Outline each Plasmodium falciparum-infected red blood cell.
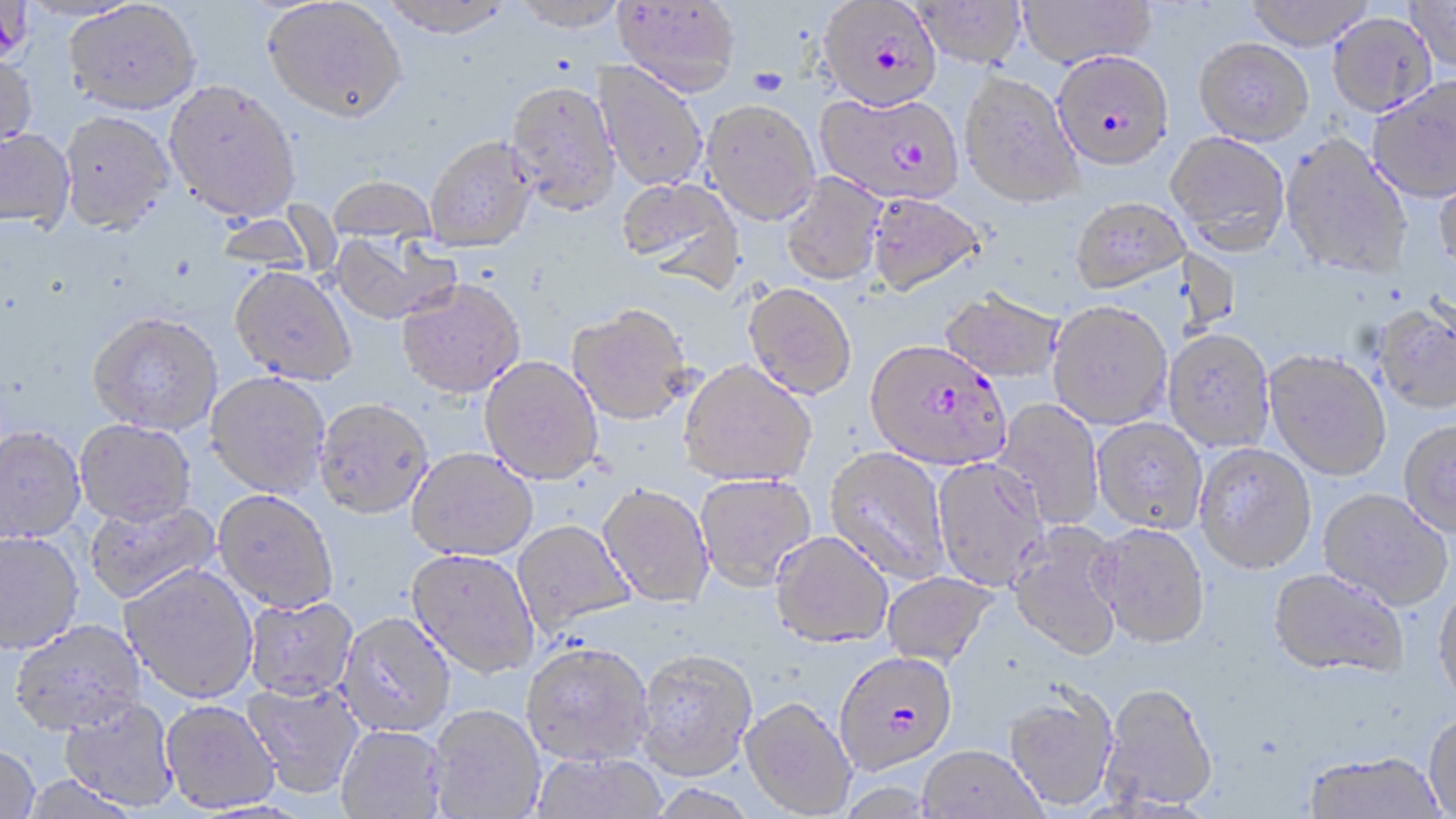

Approximate bounding boxes as named x1/y1/x2/y2 corners in pixels.
Plasmodium falciparum-infected red blood cells: (x1=818, y1=0, x2=942, y2=112), (x1=1055, y1=50, x2=1170, y2=169), (x1=815, y1=91, x2=965, y2=204), (x1=866, y1=340, x2=1011, y2=470), (x1=834, y1=651, x2=959, y2=775).

slide-level diagnosis = Plasmodium falciparum
stain = May-Grünwald-Giemsa
magnification = 1000x
preparation = thin blood smear
uninfected red blood cell locations = approximate bounding boxes as named x1/y1/x2/y2 corners in pixels: (x1=263, y1=0, x2=408, y2=124), (x1=377, y1=0, x2=515, y2=40), (x1=509, y1=0, x2=630, y2=34), (x1=613, y1=0, x2=740, y2=98), (x1=1017, y1=0, x2=1156, y2=68), (x1=1243, y1=0, x2=1376, y2=49), (x1=64, y1=1, x2=201, y2=114), (x1=913, y1=1, x2=1027, y2=69), (x1=1407, y1=1, x2=1455, y2=73), (x1=1328, y1=12, x2=1436, y2=117), (x1=1194, y1=36, x2=1313, y2=144), (x1=0, y1=52, x2=37, y2=155), (x1=593, y1=62, x2=708, y2=192), (x1=959, y1=70, x2=1082, y2=207), (x1=1367, y1=75, x2=1456, y2=203), (x1=163, y1=80, x2=301, y2=223), (x1=505, y1=82, x2=620, y2=217), (x1=702, y1=100, x2=821, y2=226), (x1=58, y1=111, x2=176, y2=234), (x1=0, y1=129, x2=76, y2=233), (x1=1166, y1=131, x2=1291, y2=255), (x1=1281, y1=134, x2=1413, y2=278), (x1=425, y1=137, x2=537, y2=253), (x1=1434, y1=164, x2=1456, y2=272), (x1=781, y1=172, x2=886, y2=286), (x1=328, y1=176, x2=437, y2=244), (x1=618, y1=178, x2=744, y2=290), (x1=867, y1=193, x2=987, y2=296), (x1=1070, y1=196, x2=1191, y2=293), (x1=329, y1=231, x2=460, y2=326), (x1=230, y1=267, x2=356, y2=385), (x1=397, y1=279, x2=526, y2=399), (x1=742, y1=283, x2=857, y2=400), (x1=940, y1=289, x2=1064, y2=382), (x1=1047, y1=300, x2=1173, y2=429), (x1=1373, y1=303, x2=1456, y2=413), (x1=568, y1=305, x2=693, y2=425), (x1=88, y1=314, x2=223, y2=436), (x1=1164, y1=328, x2=1276, y2=452), (x1=1265, y1=350, x2=1391, y2=480), (x1=479, y1=356, x2=604, y2=486), (x1=679, y1=361, x2=817, y2=487), (x1=205, y1=373, x2=330, y2=499), (x1=992, y1=398, x2=1105, y2=530), (x1=313, y1=399, x2=433, y2=522), (x1=1092, y1=417, x2=1208, y2=533), (x1=1399, y1=419, x2=1456, y2=537), (x1=75, y1=421, x2=197, y2=528), (x1=0, y1=428, x2=86, y2=544), (x1=1194, y1=443, x2=1316, y2=574), (x1=825, y1=447, x2=950, y2=583), (x1=407, y1=449, x2=538, y2=563), (x1=932, y1=457, x2=1049, y2=590), (x1=695, y1=473, x2=817, y2=591), (x1=597, y1=484, x2=714, y2=609), (x1=1319, y1=488, x2=1453, y2=610), (x1=213, y1=492, x2=338, y2=614), (x1=86, y1=499, x2=221, y2=605), (x1=512, y1=520, x2=635, y2=636), (x1=1007, y1=521, x2=1126, y2=660), (x1=1091, y1=523, x2=1211, y2=648), (x1=770, y1=531, x2=894, y2=648), (x1=0, y1=533, x2=83, y2=654), (x1=405, y1=550, x2=540, y2=680), (x1=120, y1=565, x2=259, y2=705), (x1=1268, y1=569, x2=1408, y2=679), (x1=882, y1=571, x2=998, y2=667), (x1=1433, y1=583, x2=1456, y2=710), (x1=244, y1=596, x2=359, y2=702), (x1=336, y1=614, x2=457, y2=739), (x1=8, y1=620, x2=146, y2=737), (x1=521, y1=642, x2=653, y2=766), (x1=634, y1=648, x2=758, y2=781), (x1=242, y1=679, x2=366, y2=800), (x1=1099, y1=682, x2=1219, y2=811), (x1=1003, y1=686, x2=1118, y2=812), (x1=741, y1=696, x2=857, y2=817), (x1=58, y1=698, x2=180, y2=812), (x1=160, y1=701, x2=281, y2=814), (x1=428, y1=706, x2=546, y2=819), (x1=1423, y1=711, x2=1456, y2=818), (x1=336, y1=726, x2=448, y2=819), (x1=0, y1=745, x2=40, y2=819), (x1=918, y1=745, x2=1047, y2=819), (x1=530, y1=751, x2=667, y2=818), (x1=1305, y1=751, x2=1446, y2=819)
image size = 1456×819 pixels
field of view = one of a larger specimen
modality = optical microscopy